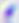

{
  "modality": "micrograph",
  "identification": "Toxoplasma gondii",
  "magnification": "400x"
}